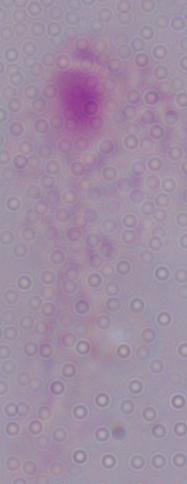

{
  "modality": "micrograph",
  "magnification": "1000x",
  "identification": "trichomonad"
}